Assess this cell for malaria.
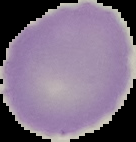
Uninfected.

Summary:
  - Image size: 136×142 pixels
  - Preparation: thin blood smear
  - Image type: segmented cell region on a black background